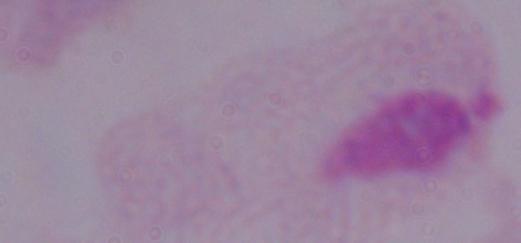

A trichomonad is shown. Photomicrograph. Captured at 1000x magnification.